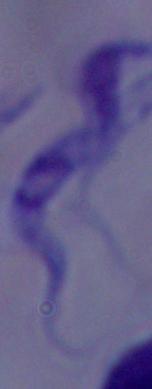
identification = trypanosome
magnification = 1000x
modality = photomicrograph